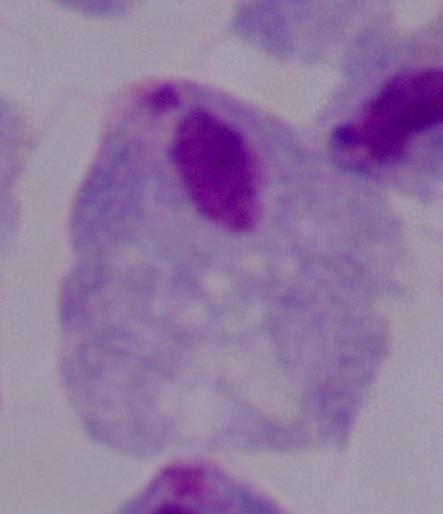

Summary:
  - Magnification: 1000x
  - Modality: photomicrograph
  - Identification: trichomonad